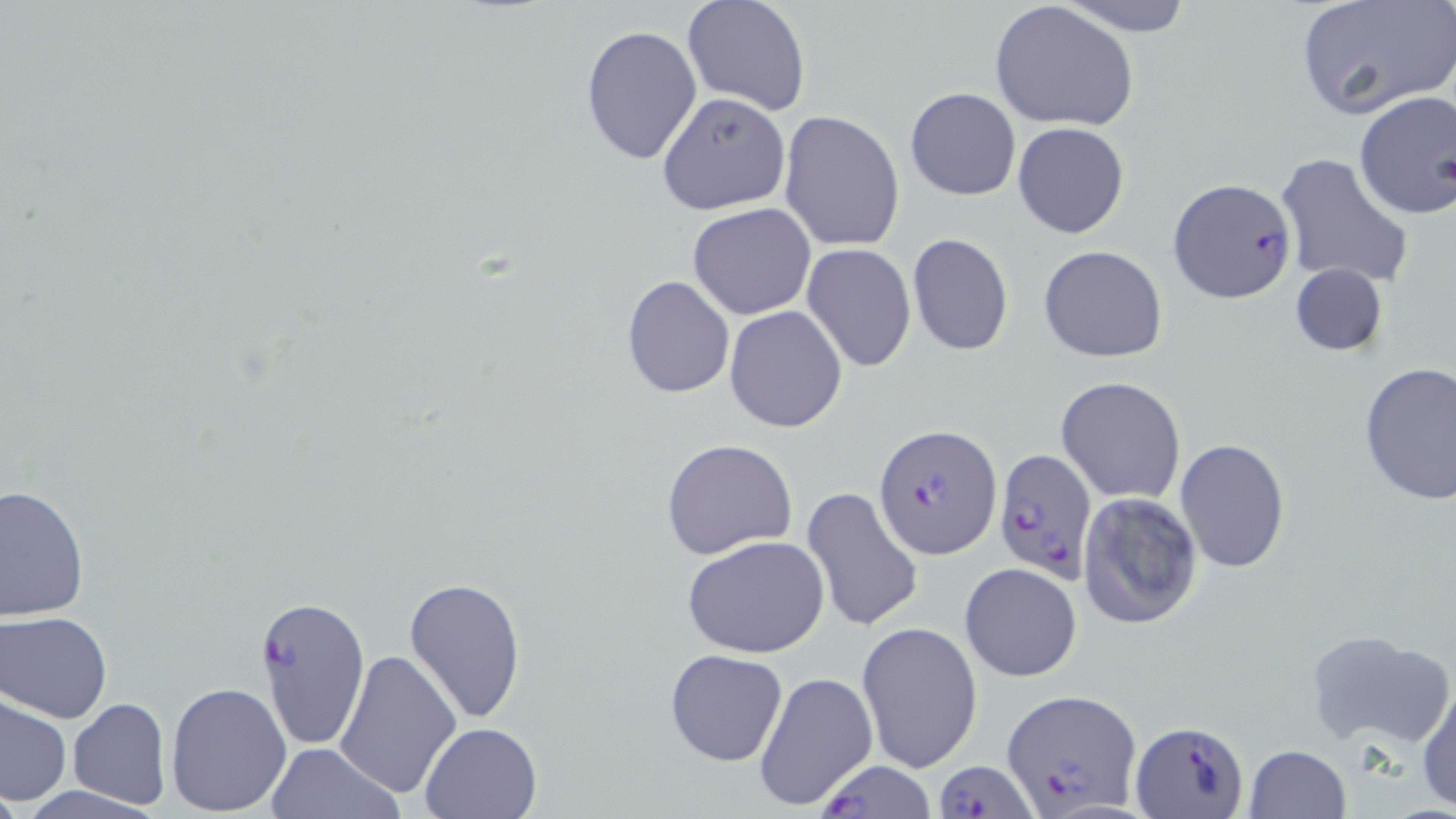
Summary:
  - Coordinate format: approximate bounding boxes as [x1, y1, x2, y2] in pixels
  - Plasmodium falciparum-infected red blood cell locations: [1168, 178, 1295, 303], [875, 424, 1001, 558], [992, 448, 1097, 583], [253, 595, 370, 751], [1004, 688, 1141, 814], [1131, 721, 1248, 816], [810, 758, 941, 818], [932, 759, 1037, 819]
  - Uninfected red blood cell locations: [682, 0, 811, 117], [1053, 0, 1197, 35], [1293, 1, 1456, 120], [989, 2, 1140, 135], [581, 24, 703, 165], [904, 87, 1021, 200], [1353, 89, 1456, 221], [657, 90, 791, 214], [779, 109, 906, 253], [1013, 122, 1129, 239], [1274, 152, 1416, 290], [687, 203, 816, 319], [906, 233, 1013, 355], [801, 244, 917, 372], [1039, 245, 1168, 364], [1287, 262, 1388, 359], [621, 275, 734, 398], [723, 305, 849, 433], [1357, 361, 1456, 505], [1055, 376, 1187, 503], [660, 437, 798, 559], [1174, 437, 1290, 574], [0, 484, 89, 620], [800, 487, 924, 631], [1079, 493, 1203, 630], [681, 534, 831, 660], [959, 563, 1082, 682], [403, 575, 527, 726], [360, 607, 513, 782], [1, 611, 112, 721], [856, 620, 983, 773], [1303, 629, 1453, 749], [663, 647, 789, 767], [334, 649, 461, 800], [755, 671, 877, 809], [1417, 680, 1456, 814], [165, 681, 292, 813], [1, 697, 71, 805], [67, 697, 169, 810], [420, 720, 545, 818], [265, 741, 403, 819], [1243, 744, 1350, 819]
  - Slide-level diagnosis: Plasmodium falciparum
  - Field of view: one of a larger specimen
  - Stain: May-Grünwald-Giemsa
  - Modality: optical microscopy
  - Magnification: 1000x
  - Image size: 1456×819 pixels
  - Preparation: thin blood smear